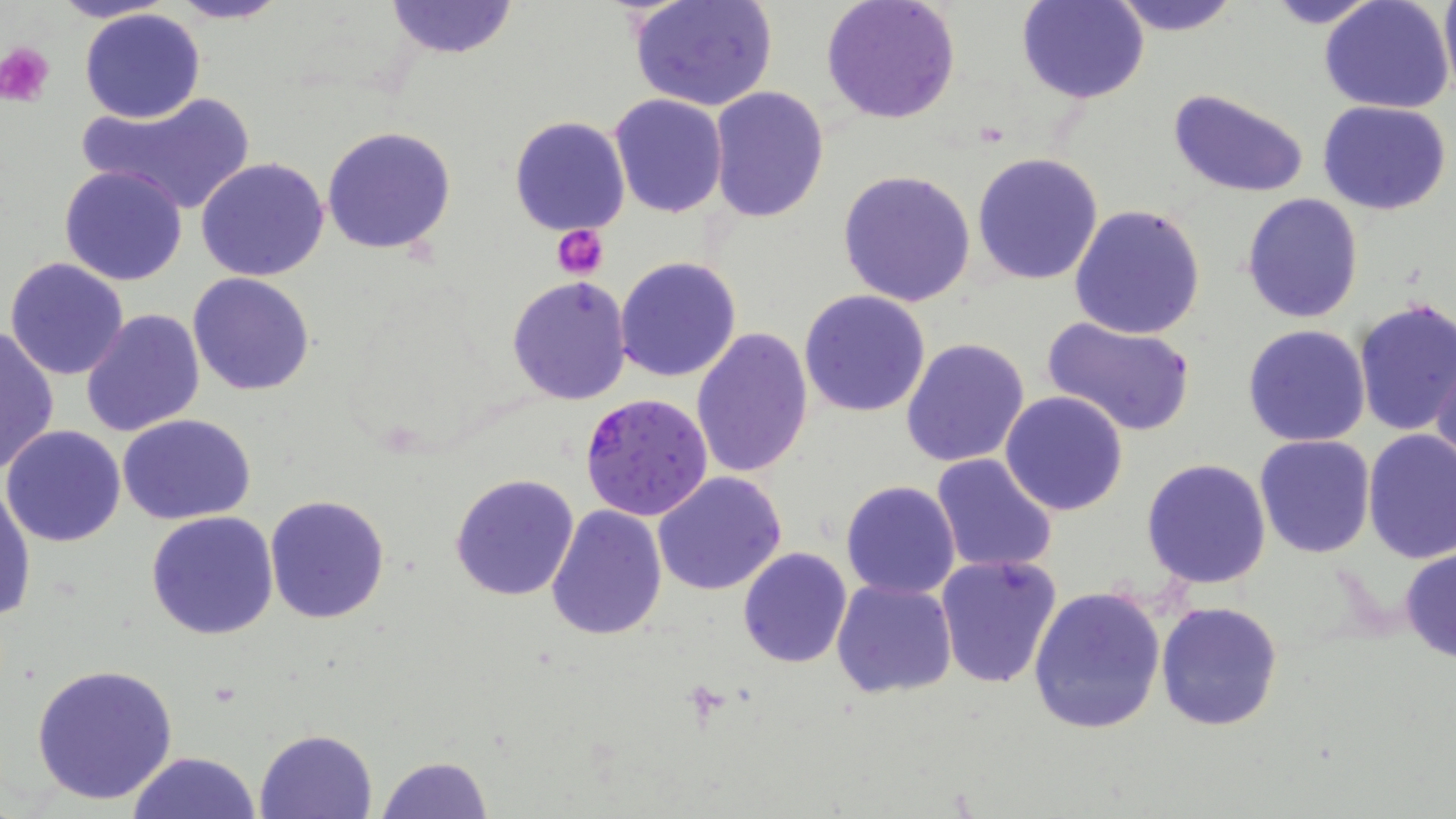

Summary:
  - Coordinate format: approximate bounding boxes as named x1/y1/x2/y2 corners in pixels
  - Platelet locations: (x1=1, y1=44, x2=55, y2=105), (x1=553, y1=226, x2=609, y2=280)
  - Uninfected red blood cell locations: (x1=51, y1=0, x2=178, y2=24), (x1=167, y1=0, x2=289, y2=24), (x1=384, y1=0, x2=516, y2=60), (x1=821, y1=0, x2=961, y2=125), (x1=1016, y1=0, x2=1149, y2=103), (x1=1106, y1=0, x2=1242, y2=37), (x1=1259, y1=0, x2=1387, y2=29), (x1=1437, y1=0, x2=1456, y2=97), (x1=630, y1=1, x2=777, y2=112), (x1=1319, y1=1, x2=1456, y2=115), (x1=78, y1=9, x2=207, y2=123), (x1=709, y1=86, x2=830, y2=224), (x1=1169, y1=89, x2=1311, y2=199), (x1=73, y1=92, x2=257, y2=217), (x1=607, y1=94, x2=729, y2=218), (x1=1317, y1=100, x2=1452, y2=215), (x1=508, y1=115, x2=632, y2=237), (x1=320, y1=125, x2=457, y2=256), (x1=973, y1=151, x2=1105, y2=286), (x1=195, y1=157, x2=330, y2=281), (x1=58, y1=164, x2=188, y2=286), (x1=838, y1=169, x2=976, y2=307), (x1=1242, y1=193, x2=1363, y2=324), (x1=1069, y1=204, x2=1206, y2=340), (x1=615, y1=256, x2=742, y2=383), (x1=4, y1=257, x2=130, y2=381), (x1=187, y1=272, x2=317, y2=396), (x1=506, y1=276, x2=634, y2=406), (x1=799, y1=290, x2=931, y2=416), (x1=1352, y1=300, x2=1456, y2=436), (x1=78, y1=307, x2=205, y2=438), (x1=1039, y1=315, x2=1198, y2=441), (x1=0, y1=324, x2=59, y2=474), (x1=1241, y1=325, x2=1371, y2=447), (x1=691, y1=327, x2=814, y2=479), (x1=901, y1=337, x2=1031, y2=468), (x1=1431, y1=352, x2=1456, y2=474), (x1=1000, y1=391, x2=1130, y2=515), (x1=117, y1=413, x2=258, y2=526), (x1=3, y1=425, x2=127, y2=548), (x1=1362, y1=430, x2=1456, y2=563), (x1=1254, y1=434, x2=1377, y2=558), (x1=930, y1=453, x2=1058, y2=574), (x1=1141, y1=457, x2=1274, y2=591), (x1=653, y1=471, x2=787, y2=594), (x1=450, y1=472, x2=580, y2=602), (x1=841, y1=480, x2=961, y2=600), (x1=0, y1=483, x2=35, y2=624), (x1=264, y1=494, x2=391, y2=626), (x1=546, y1=506, x2=668, y2=641), (x1=146, y1=512, x2=279, y2=641), (x1=1398, y1=544, x2=1456, y2=666), (x1=738, y1=545, x2=852, y2=667), (x1=935, y1=554, x2=1063, y2=689), (x1=832, y1=578, x2=958, y2=700), (x1=1025, y1=584, x2=1168, y2=735), (x1=1156, y1=600, x2=1283, y2=730), (x1=31, y1=663, x2=178, y2=806), (x1=256, y1=728, x2=376, y2=818), (x1=127, y1=751, x2=264, y2=819), (x1=375, y1=755, x2=491, y2=819)
  - Plasmodium falciparum-infected red blood cell locations: (x1=578, y1=393, x2=715, y2=522)
  - Slide-level diagnosis: Plasmodium falciparum
  - Stain: May-Grünwald-Giemsa
  - Image size: 1456×819 pixels
  - Field of view: single
  - Magnification: 1000x
  - Preparation: thin blood film
  - Modality: optical microscopy